Give the position of every malaria parasite.
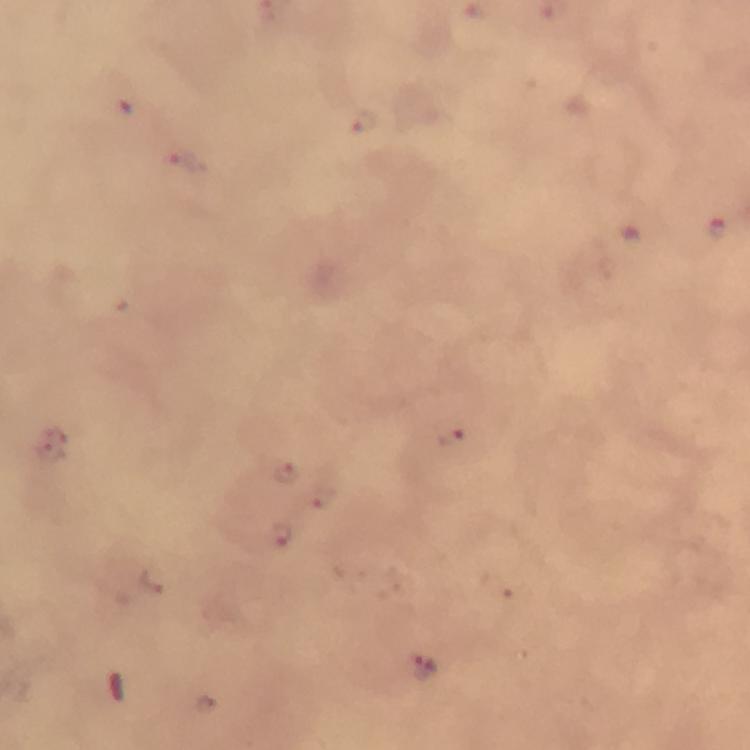

Approximate centers as {x, y} in pixels.
Malaria parasites: {126, 111}, {363, 123}, {185, 159}, {718, 230}, {449, 436}, {286, 469}, {320, 496}, {283, 535}, {427, 669}.

context = from a diagnostic examination for malaria
stain = Giemsa
image size = 750×750 pixels
preparation = thick blood smear
magnification = 100x
capture = smartphone camera through the microscope
immersion oil = used
cropped from = a single field of view